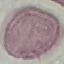
Malaria status: uninfected. Cell patch, automatically extracted from a larger field of view and resized to 64 × 64 pixels. Acquired by smartphone through the microscope eyepiece. Thin blood smear. Giemsa stain.